Give the position of every Plasmodium parasite.
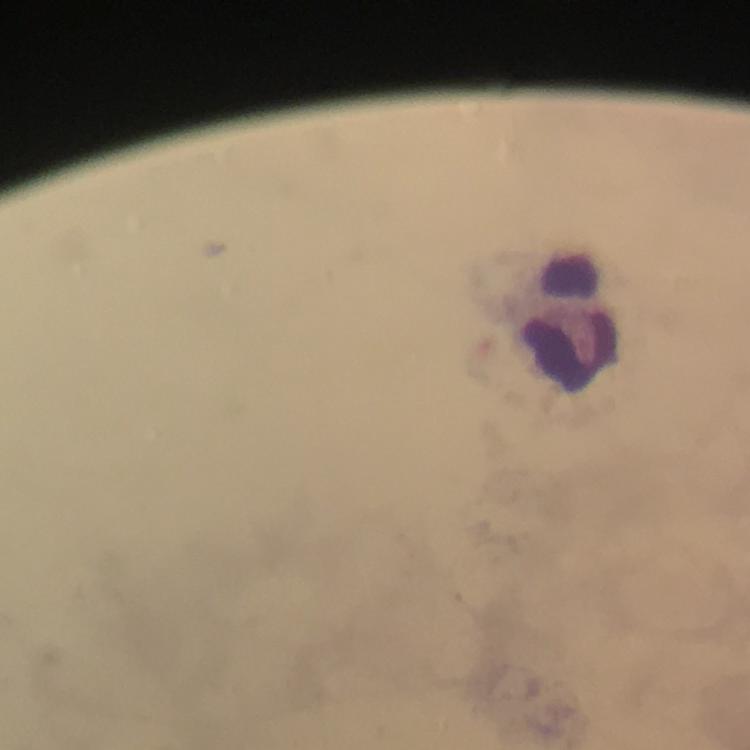

No Plasmodium parasites detected.

Approximate centers as {x, y} in pixels. Leukocyte locations: {570, 322}. Giemsa-stained preparation. Immersion oil applied. Thick blood film. From a diagnostic examination for malaria. Cropped region of a single field of view. Image is 750×750 pixels. Smartphone photograph taken through a microscope. 100x magnification.